Classify this cell by malaria status.
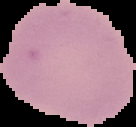
Uninfected.

{
  "image_size": "136×127 pixels",
  "preparation": "thin blood smear",
  "image_type": "segmented cell region with the area outside set to black"
}